Give a bounding box for every parasitised red blood cell.
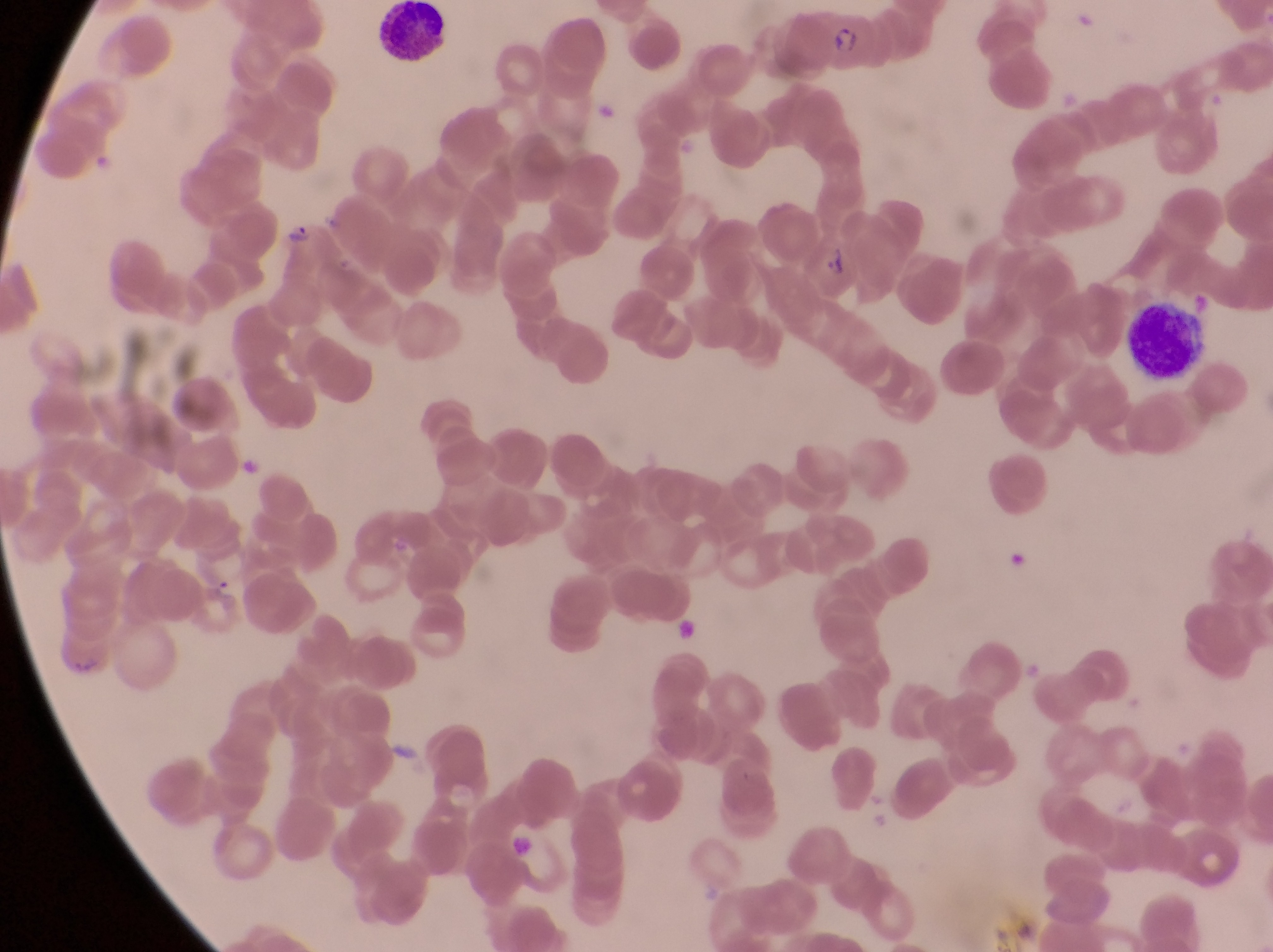
Approximate bounding boxes as [left, top, right, bottom] in pixels.
Parasitised red blood cells: [816, 2, 878, 77], [816, 235, 855, 302].

country: Uganda
artifact_platelet_like_body_stain_precipitate_or_debris_locations: 'approximate bounding boxes as [left, top, right, bottom] in pixels: [1011, 542, 1031, 581], [667, 610, 700, 647], [512, 826, 547, 871]'
leukocyte_locations: 'approximate bounding boxes as [left, top, right, bottom] in pixels: [372, 2, 455, 67], [1133, 292, 1210, 384]'
trophozoite_locations: 'approximate bounding boxes as [left, top, right, bottom] in pixels: [285, 212, 313, 252], [211, 575, 239, 608]'
image_size: 1273×952 pixels
magnification: 1000x
preparation: thin blood film
field_of_view: single
capture: smartphone photograph through the eyepiece of an Olympus CX-23 microscope